Identify the parasite.
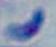

Toxoplasma gondii.

Photomicrograph. Captured at 1000x magnification.